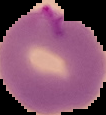
preparation = thin blood film
result = malaria parasites detected
image size = 106×115 pixels
image type = segmented cell region on a black background